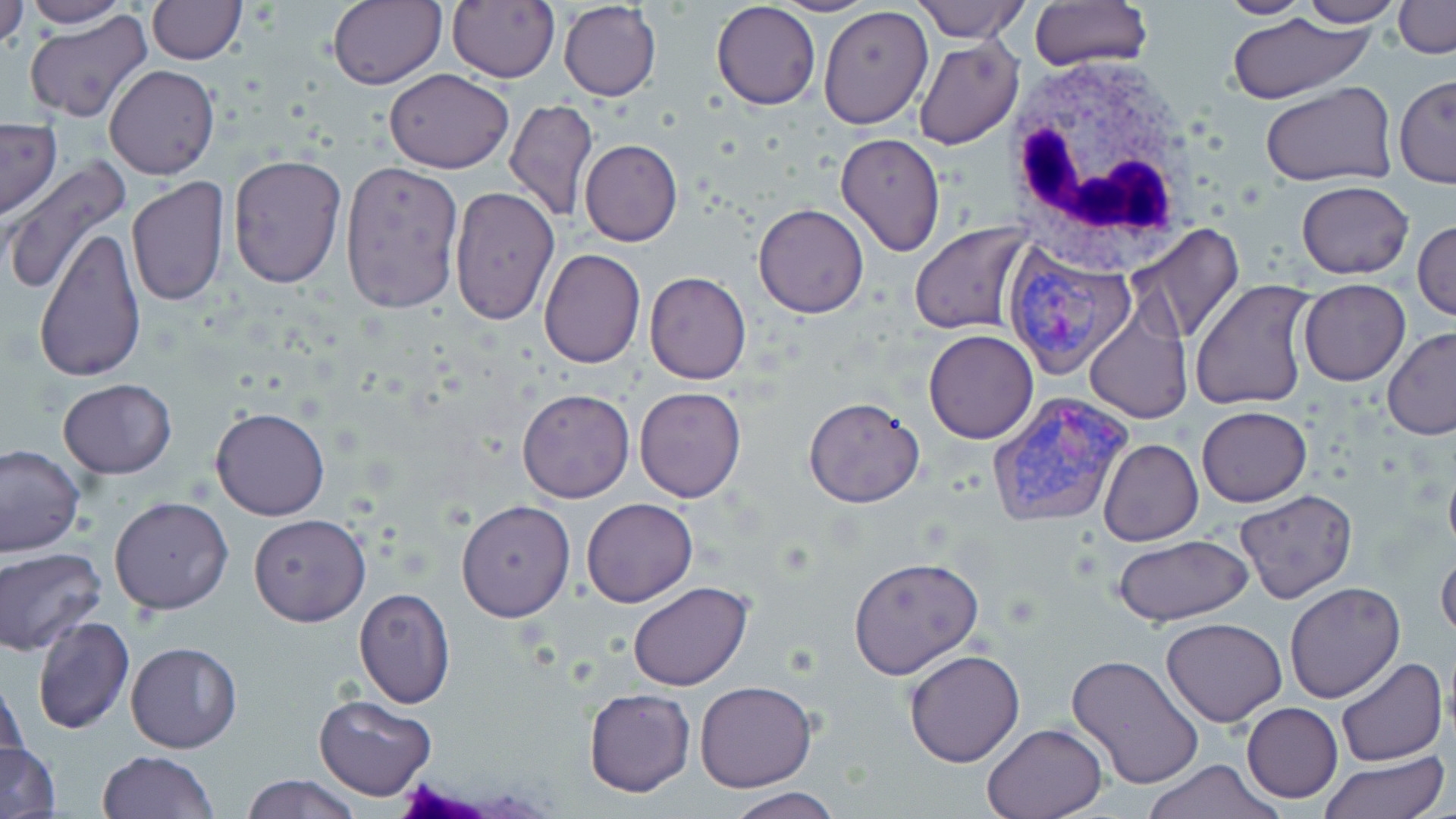
{
  "slide_level_diagnosis": "Plasmodium vivax",
  "field_of_view": "one of a larger specimen",
  "magnification": "1000x",
  "uninfected_red_blood_cell_locations": "approximate bounding boxes as named x1/y1/x2/y2 corners in pixels: (x1=24, y1=0, x2=128, y2=28), (x1=147, y1=0, x2=245, y2=65), (x1=447, y1=0, x2=560, y2=85), (x1=769, y1=0, x2=876, y2=17), (x1=914, y1=0, x2=1031, y2=41), (x1=1028, y1=0, x2=1151, y2=71), (x1=1217, y1=0, x2=1312, y2=19), (x1=1298, y1=0, x2=1404, y2=26), (x1=0, y1=1, x2=27, y2=51), (x1=327, y1=1, x2=445, y2=89), (x1=1394, y1=1, x2=1455, y2=57), (x1=558, y1=2, x2=661, y2=101), (x1=713, y1=2, x2=821, y2=109), (x1=818, y1=5, x2=934, y2=129), (x1=1225, y1=11, x2=1379, y2=103), (x1=24, y1=13, x2=153, y2=123), (x1=913, y1=38, x2=1025, y2=151), (x1=105, y1=64, x2=219, y2=179), (x1=385, y1=69, x2=512, y2=173), (x1=1394, y1=74, x2=1455, y2=187), (x1=1261, y1=83, x2=1396, y2=189), (x1=505, y1=98, x2=599, y2=224), (x1=0, y1=119, x2=62, y2=218), (x1=836, y1=133, x2=945, y2=257), (x1=579, y1=139, x2=682, y2=246), (x1=227, y1=154, x2=346, y2=290), (x1=340, y1=157, x2=464, y2=316), (x1=2, y1=160, x2=131, y2=298), (x1=127, y1=176, x2=229, y2=306), (x1=1295, y1=181, x2=1414, y2=278), (x1=448, y1=185, x2=558, y2=327), (x1=753, y1=203, x2=870, y2=317), (x1=1414, y1=220, x2=1455, y2=322), (x1=910, y1=222, x2=1033, y2=335), (x1=1128, y1=222, x2=1246, y2=344), (x1=35, y1=226, x2=146, y2=383), (x1=539, y1=248, x2=644, y2=368), (x1=644, y1=271, x2=751, y2=385), (x1=1192, y1=278, x2=1319, y2=413), (x1=1298, y1=279, x2=1410, y2=385), (x1=1084, y1=308, x2=1192, y2=424), (x1=1382, y1=326, x2=1456, y2=439), (x1=923, y1=330, x2=1038, y2=444), (x1=58, y1=379, x2=177, y2=478), (x1=635, y1=386, x2=747, y2=502), (x1=517, y1=388, x2=635, y2=503), (x1=803, y1=396, x2=926, y2=508), (x1=211, y1=406, x2=330, y2=521), (x1=1197, y1=406, x2=1311, y2=506), (x1=1098, y1=438, x2=1203, y2=546), (x1=0, y1=444, x2=84, y2=558), (x1=1235, y1=491, x2=1357, y2=604), (x1=110, y1=496, x2=234, y2=615), (x1=582, y1=497, x2=698, y2=607), (x1=457, y1=500, x2=575, y2=623), (x1=249, y1=513, x2=370, y2=626), (x1=1113, y1=536, x2=1253, y2=627), (x1=1437, y1=545, x2=1456, y2=646), (x1=2, y1=547, x2=108, y2=655), (x1=848, y1=557, x2=983, y2=678), (x1=627, y1=581, x2=752, y2=691), (x1=1283, y1=582, x2=1404, y2=703), (x1=354, y1=589, x2=455, y2=708), (x1=32, y1=615, x2=133, y2=735), (x1=1161, y1=616, x2=1286, y2=726), (x1=125, y1=641, x2=243, y2=752), (x1=904, y1=648, x2=1026, y2=767), (x1=1067, y1=656, x2=1203, y2=791), (x1=1335, y1=657, x2=1446, y2=768), (x1=1, y1=673, x2=28, y2=775), (x1=695, y1=680, x2=816, y2=791), (x1=583, y1=688, x2=694, y2=796), (x1=313, y1=693, x2=436, y2=802), (x1=1241, y1=702, x2=1343, y2=803), (x1=982, y1=721, x2=1106, y2=817), (x1=0, y1=742, x2=59, y2=818), (x1=98, y1=749, x2=217, y2=819), (x1=1318, y1=751, x2=1450, y2=818), (x1=1141, y1=759, x2=1285, y2=819), (x1=242, y1=774, x2=360, y2=819), (x1=721, y1=787, x2=845, y2=819)",
  "image_size": "1456×819 pixels",
  "white_blood_cell_locations": "approximate bounding boxes as named x1/y1/x2/y2 corners in pixels: (x1=1003, y1=56, x2=1208, y2=260)",
  "stain": "May-Grünwald-Giemsa",
  "modality": "light microscopy",
  "plasmodium_vivax_infected_red_blood_cell_locations": "approximate bounding boxes as named x1/y1/x2/y2 corners in pixels: (x1=1005, y1=241, x2=1138, y2=378), (x1=984, y1=391, x2=1139, y2=531)",
  "preparation": "thin blood smear"
}